Assess this cell for malaria.
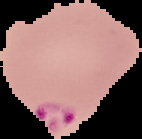
It is parasitized.

image type = segmented cell region with the area outside set to black
preparation = thin blood film
image size = 142×139 pixels